Locate every malaria parasite.
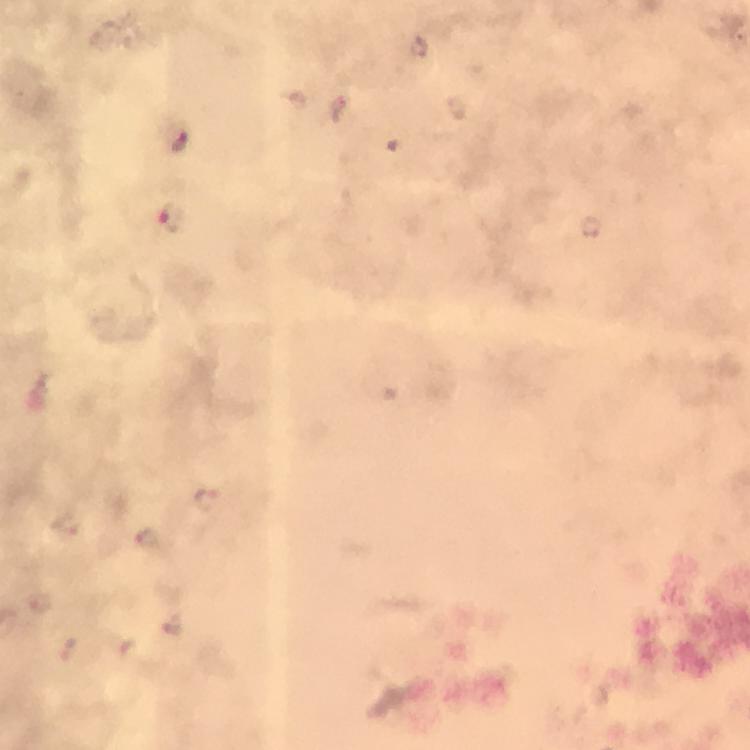

Approximate centers as (x, y) in pixels.
Malaria parasites: (208, 500), (66, 524), (149, 539), (41, 604), (68, 651).

cropped from = a single field of view
magnification = 100x
immersion oil = used
context = from a malaria diagnostic workup
capture = smartphone photograph through a microscope
stain = Giemsa
image size = 750×750 pixels
preparation = thick blood smear